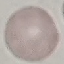

Summary:
  - Malaria status: uninfected
  - Image type: cell patch, automatically extracted from a larger field of view and resized to 64 × 64 pixels
  - Capture: smartphone through the microscope eyepiece
  - Stain: Giemsa
  - Preparation: thin blood film